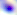
Summary:
  - Identification: Toxoplasma gondii
  - Modality: micrograph
  - Magnification: 400x